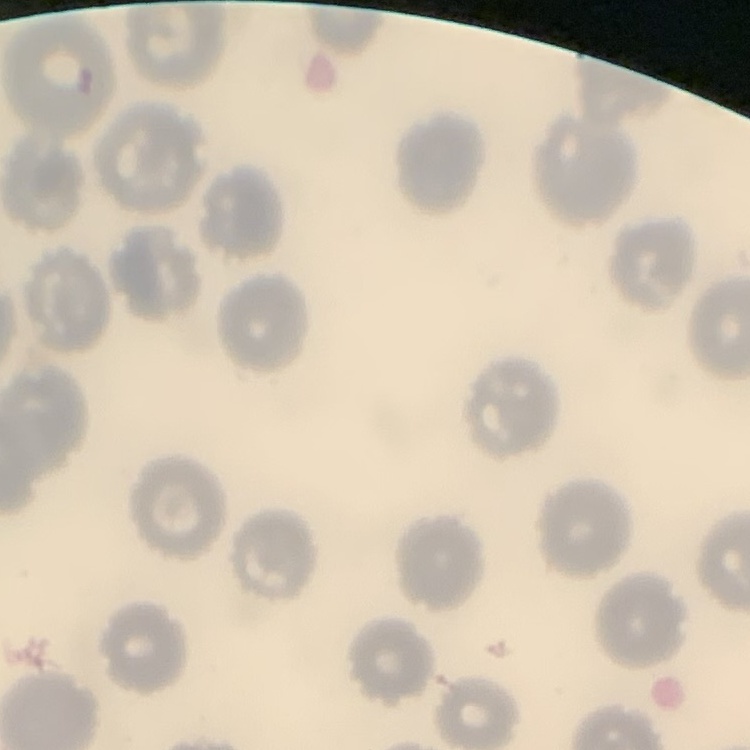

erythrocyte_morphology: no rouleaux formation
preparation: thin blood smear
stain: Field's or Giemsa
image_type: one tile cut from a larger photomicrograph